State which parasite is depicted.
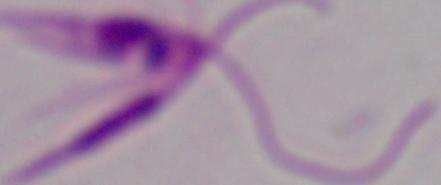
This is Leishmania.

magnification = 1000x
modality = micrograph